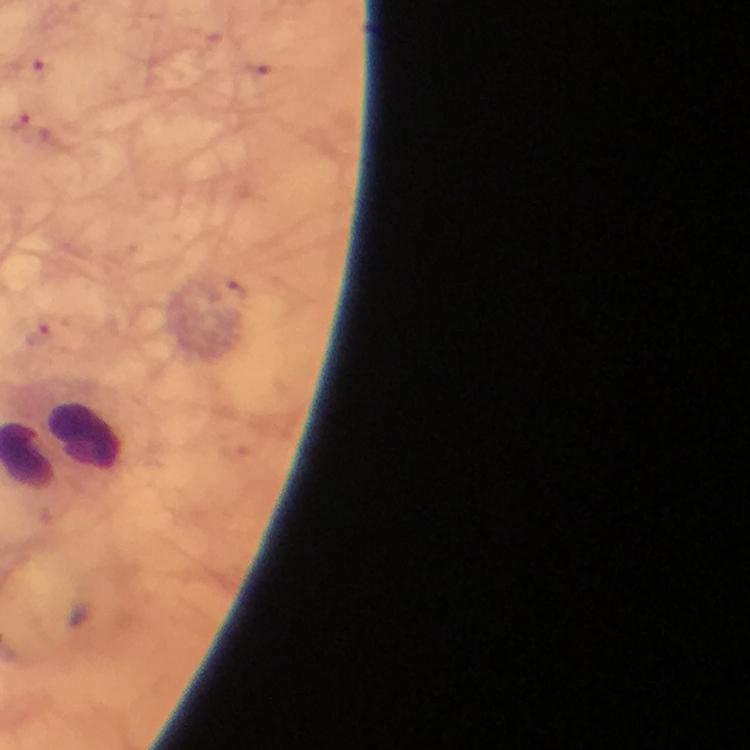

plasmodium_parasites: none seen
context: from a malaria diagnostic workup
stain: Giemsa
preparation: thick smear
leukocyte_locations: 'approximate centers as (x, y) in pixels: (83, 437)'
capture: smartphone photograph through a microscope
immersion_oil: used
cropped_from: a single field of view
image_size: 750×750 pixels
magnification: 100x